Describe the morphology of the red blood cells.
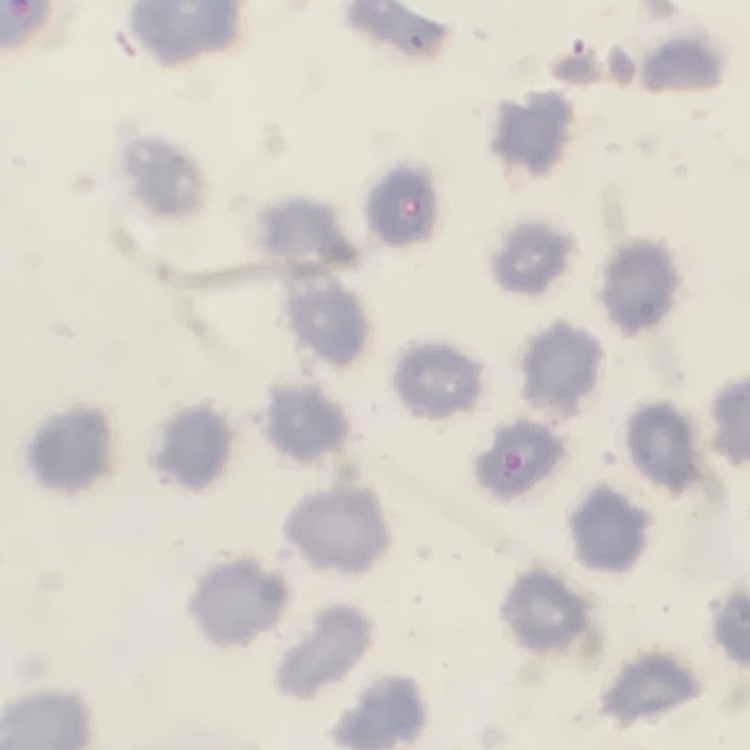
No rouleaux formation.

Thin blood smear. Stained with either Field's or Giemsa. One tile cut from a larger photomicrograph.